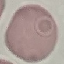
Result: no malaria parasites detected. Thin blood smear. Acquired by smartphone through the microscope eyepiece. Automatically extracted cell patch, resized to 64 × 64 pixels. Giemsa-stained preparation.